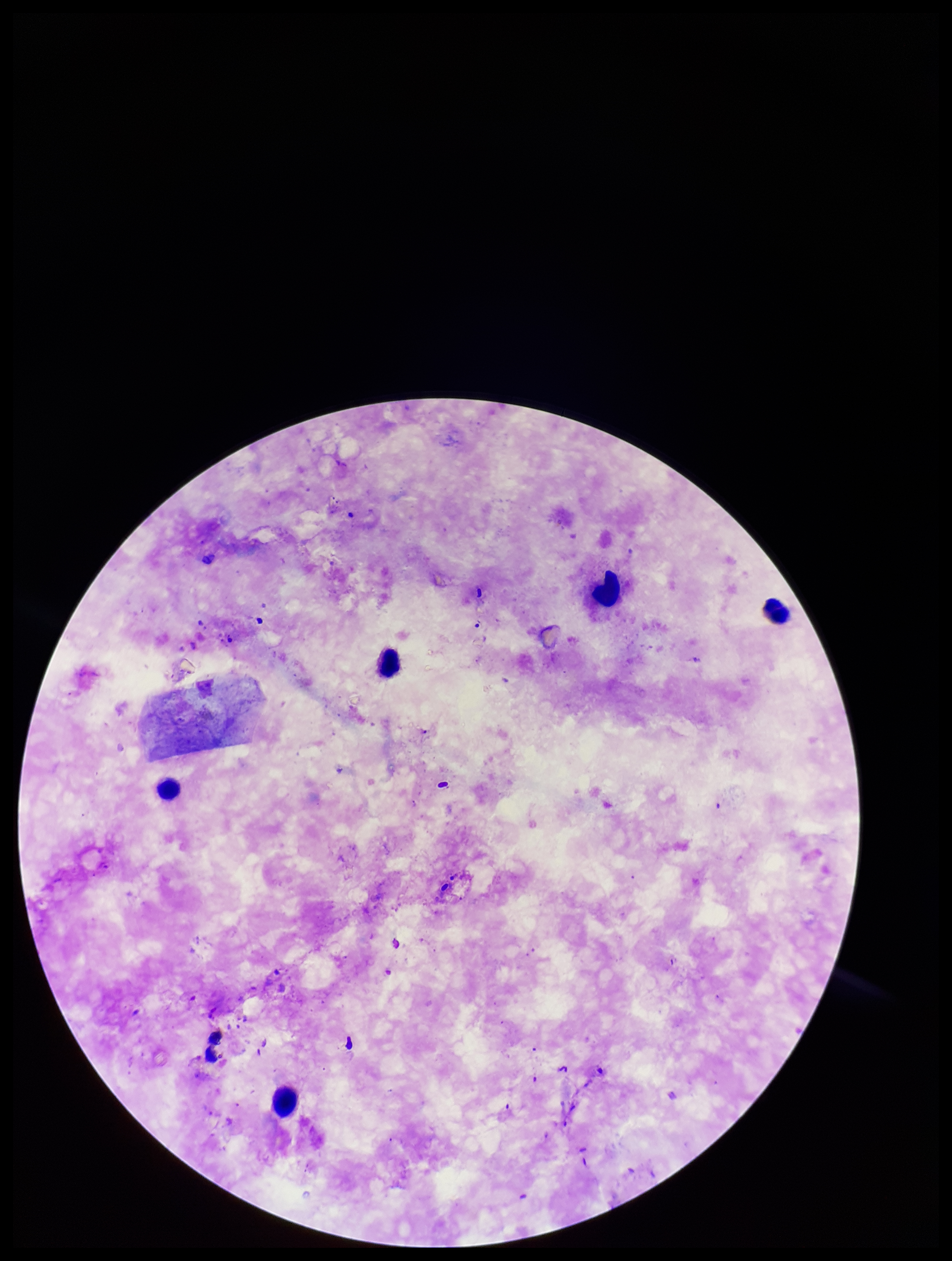

Summary:
  - Patient malaria status: negative
  - Plasmodium parasites: none detected
  - Field of view: one from this slide
  - Parasite count: 0
  - Image size: 952×1261 pixels
  - Leukocyte count: 5
  - Capture: smartphone photograph through the microscope eyepiece
  - Stain: Giemsa
  - Preparation: thick blood smear